Identify the cell.
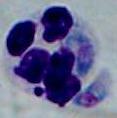

A leukocyte.

modality = photomicrograph
magnification = 1000x